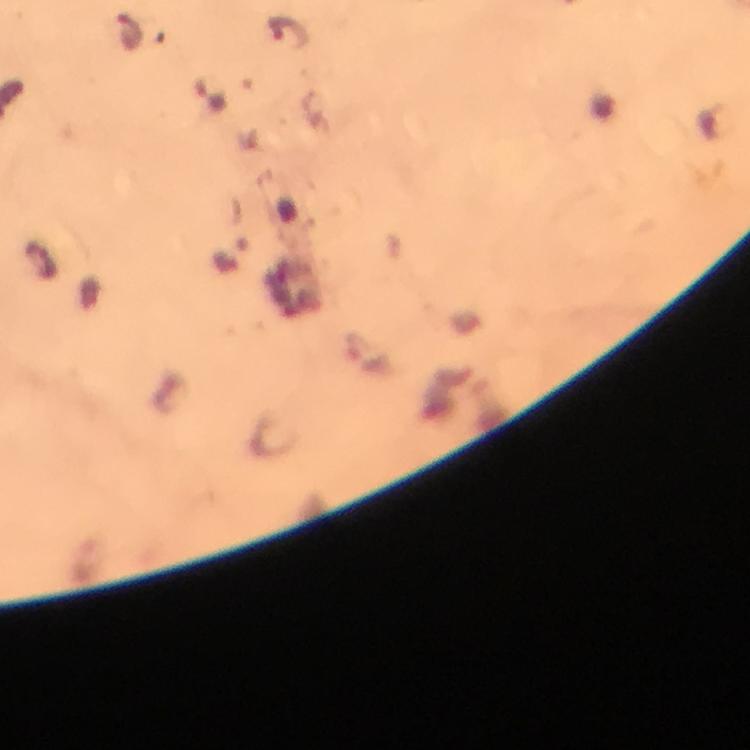

Approximate centers as [x, y] in pixels. Malaria parasite locations: [132, 33], [287, 33], [210, 94], [367, 359]. Cropped region of a single field of view. Thick blood film. Photographed with a smartphone mounted on the microscope. Image is 750×750 pixels. From a diagnostic examination for malaria. Immersion oil applied. 100x magnification. Giemsa stain.